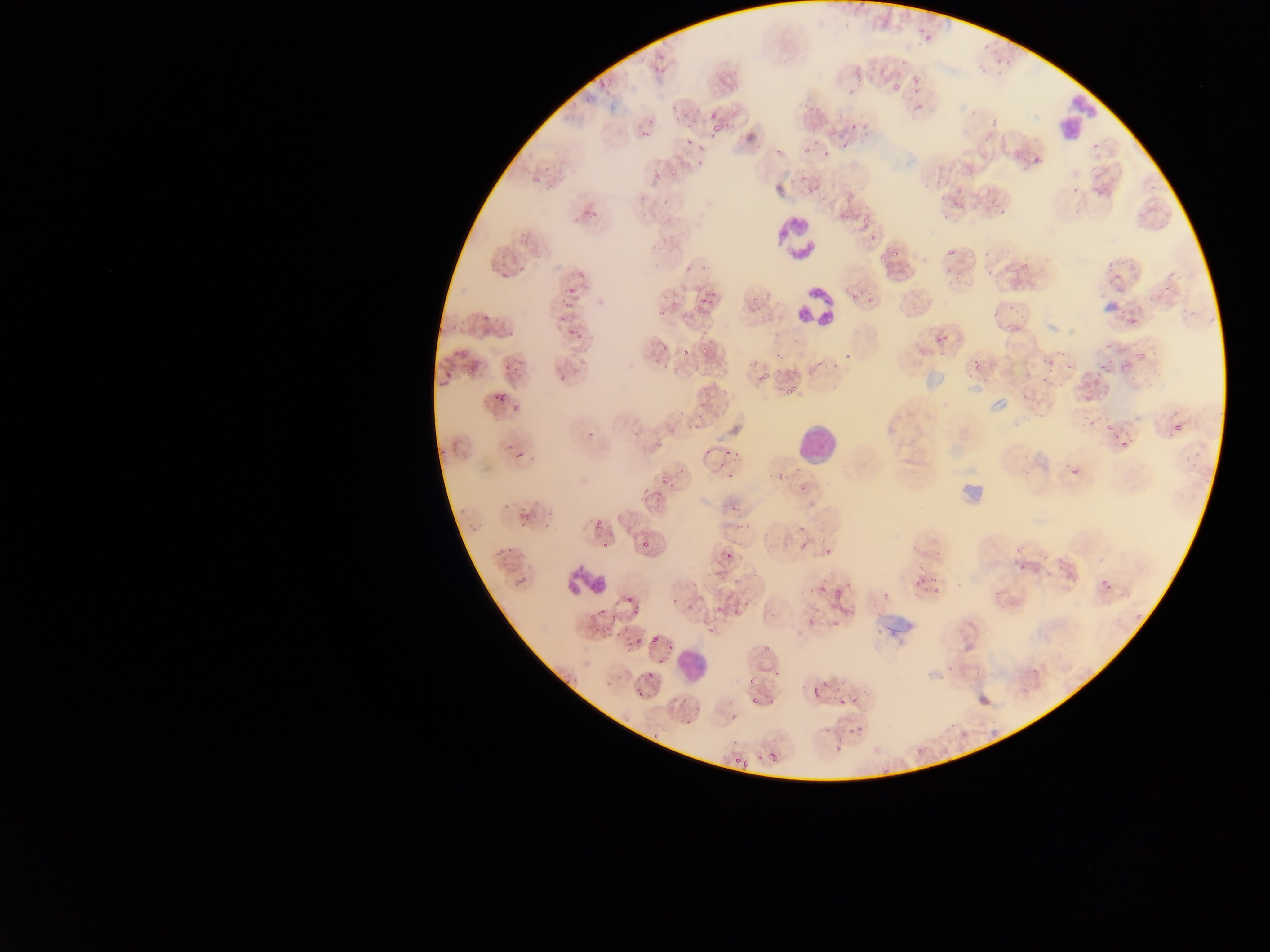

Approximate bounding boxes as {left, top, right, bottom} in pixels.
Summary:
  - Leukocyte locations: {1060, 93, 1098, 144}, {775, 216, 822, 260}, {791, 279, 835, 326}, {797, 429, 834, 462}, {563, 565, 608, 597}, {675, 636, 715, 686}
  - Malaria parasite locations: {916, 27, 941, 44}, {979, 42, 994, 54}, {994, 57, 1002, 64}, {655, 58, 669, 76}, {899, 58, 910, 68}, {1005, 62, 1018, 67}, {976, 64, 984, 73}, {991, 71, 1008, 81}, {910, 75, 929, 83}, {590, 76, 597, 85}, {597, 80, 608, 95}, {891, 82, 902, 92}, {913, 86, 925, 95}, {582, 90, 596, 104}, {706, 102, 716, 119}, {666, 105, 676, 113}, {678, 110, 687, 124}, {990, 110, 1001, 127}, {647, 116, 658, 127}, {712, 121, 723, 133}, {641, 130, 651, 142}, {681, 131, 695, 144}, {981, 133, 995, 143}, {1032, 142, 1052, 167}, {1088, 142, 1099, 151}, {695, 145, 705, 160}, {1012, 146, 1030, 161}, {682, 147, 691, 161}, {542, 164, 551, 173}, {653, 170, 664, 181}, {936, 175, 946, 186}, {531, 176, 543, 187}, {547, 182, 556, 195}, {1070, 186, 1083, 195}, {1094, 187, 1107, 197}, {632, 191, 649, 205}, {658, 192, 671, 204}, {940, 192, 948, 201}, {953, 195, 970, 209}, {990, 198, 1003, 212}, {586, 209, 595, 218}, {941, 210, 951, 218}, {1135, 212, 1147, 220}, {568, 216, 578, 226}, {861, 216, 872, 228}, {1156, 223, 1165, 230}, {646, 237, 663, 256}, {667, 240, 679, 254}, {888, 243, 901, 257}, {982, 246, 990, 262}, {496, 247, 507, 262}, {947, 249, 959, 256}, {977, 251, 1003, 274}, {878, 255, 888, 264}, {682, 260, 694, 272}, {1012, 263, 1023, 275}, {1169, 266, 1178, 288}, {502, 267, 512, 278}, {956, 267, 964, 277}, {1112, 267, 1125, 280}, {961, 273, 977, 292}, {941, 275, 950, 290}, {1160, 283, 1173, 292}, {568, 284, 578, 299}, {849, 288, 859, 302}, {691, 291, 718, 312}, {1098, 291, 1109, 300}, {864, 293, 876, 308}, {910, 293, 927, 314}, {1148, 293, 1160, 303}, {751, 295, 760, 305}, {562, 298, 575, 309}, {669, 299, 678, 308}, {1007, 302, 1014, 311}, {1118, 306, 1132, 317}, {1179, 308, 1191, 318}, {484, 311, 492, 319}, {989, 311, 1001, 321}, {497, 312, 513, 326}, {1012, 312, 1022, 332}, {1125, 315, 1139, 325}, {558, 316, 572, 324}, {564, 326, 575, 338}, {935, 330, 946, 343}, {571, 331, 586, 341}, {1009, 338, 1016, 348}, {1136, 338, 1149, 364}, {700, 339, 713, 354}, {1104, 344, 1113, 352}, {1116, 346, 1126, 360}, {680, 348, 692, 356}, {458, 350, 474, 356}, {775, 351, 790, 368}, {1043, 351, 1057, 366}, {842, 353, 852, 359}, {452, 355, 458, 370}, {813, 356, 826, 368}, {971, 357, 982, 369}, {512, 358, 518, 374}, {1115, 360, 1133, 377}, {465, 361, 482, 377}, {501, 361, 511, 370}, {1061, 361, 1073, 373}, {716, 362, 725, 369}, {753, 362, 770, 380}, {831, 362, 837, 374}, {1096, 367, 1104, 376}, {439, 369, 450, 381}, {697, 369, 707, 378}, {966, 371, 986, 383}, {559, 375, 567, 382}, {1038, 376, 1051, 388}, {783, 380, 800, 400}, {495, 388, 512, 405}, {1018, 392, 1027, 399}, {510, 403, 522, 418}, {674, 409, 684, 417}, {693, 415, 705, 424}, {1084, 416, 1099, 427}, {1104, 416, 1118, 435}, {1171, 418, 1185, 434}, {684, 423, 693, 434}, {632, 426, 644, 438}, {586, 432, 594, 440}, {449, 440, 462, 450}, {654, 441, 664, 452}, {1119, 442, 1127, 447}, {506, 444, 515, 452}, {514, 447, 528, 461}, {706, 447, 711, 459}, {719, 447, 732, 456}, {438, 449, 448, 460}, {730, 451, 740, 462}, {1022, 453, 1032, 464}, {1187, 456, 1200, 477}, {1068, 464, 1084, 476}, {674, 465, 691, 477}, {793, 465, 804, 475}, {1021, 468, 1034, 477}, {778, 473, 787, 480}, {726, 474, 733, 485}, {658, 475, 670, 486}, {797, 481, 815, 493}, {642, 488, 650, 496}, {655, 491, 665, 504}, {726, 504, 739, 514}, {546, 505, 556, 516}, {517, 510, 529, 522}, {732, 518, 751, 532}, {595, 519, 603, 526}, {799, 523, 812, 534}, {642, 540, 654, 549}, {600, 541, 612, 552}, {766, 542, 779, 551}, {800, 542, 810, 549}, {495, 543, 514, 557}, {935, 544, 944, 562}, {824, 546, 832, 558}, {1015, 546, 1023, 555}, {728, 550, 736, 560}, {1039, 554, 1048, 565}, {1095, 557, 1106, 561}, {1012, 558, 1022, 568}, {914, 563, 924, 573}, {1056, 566, 1069, 579}, {916, 573, 931, 589}, {512, 574, 532, 591}, {1097, 575, 1115, 590}, {820, 580, 828, 596}, {931, 583, 943, 595}, {807, 585, 814, 593}, {830, 588, 843, 604}, {798, 589, 805, 598}, {991, 591, 999, 598}, {671, 593, 681, 607}, {624, 595, 635, 603}, {731, 602, 746, 615}, {597, 606, 606, 618}, {633, 606, 641, 619}, {611, 610, 620, 622}, {1132, 611, 1148, 620}, {588, 616, 598, 632}, {809, 617, 818, 628}, {834, 620, 844, 630}, {604, 621, 609, 637}, {874, 622, 887, 638}, {703, 630, 717, 639}, {615, 631, 624, 637}, {650, 632, 660, 646}, {635, 638, 644, 648}, {759, 641, 774, 658}, {665, 642, 673, 652}, {659, 653, 665, 665}, {947, 657, 957, 671}, {972, 663, 988, 675}, {560, 667, 577, 686}, {1028, 667, 1042, 680}, {774, 669, 780, 681}, {643, 670, 657, 682}, {749, 675, 766, 688}, {811, 677, 828, 699}, {839, 685, 856, 706}, {634, 690, 642, 698}, {751, 696, 759, 704}, {671, 697, 679, 707}, {767, 699, 776, 704}, {692, 704, 704, 719}, {729, 711, 738, 718}, {681, 716, 693, 725}, {825, 721, 834, 735}, {850, 724, 865, 739}, {651, 732, 656, 742}, {833, 738, 850, 752}, {916, 744, 925, 759}, {770, 753, 776, 761}, {733, 756, 739, 764}, {743, 757, 753, 773}, {882, 769, 894, 778} | approximate {x, y} pixel centers of objects too small to bound: {918, 107}, {510, 334}, {795, 370}, {766, 537}, {886, 597}, {720, 608}
  - Capture: mobile-phone photograph through a microscope
  - Image size: 1270×952 pixels
  - Preparation: thin blood smear
  - Country: Ghana
  - Field of view: single